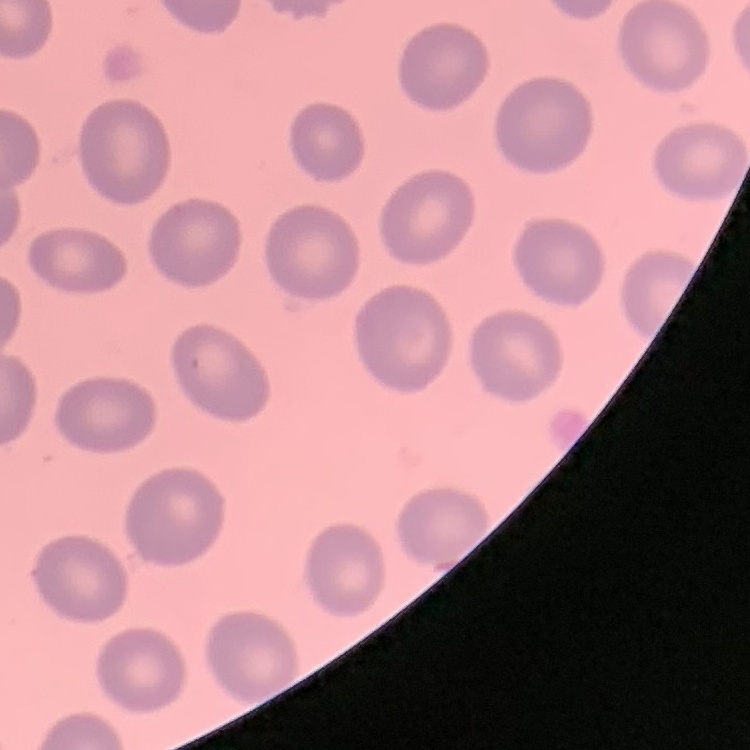

{
  "erythrocyte_morphology": "no rouleaux formation",
  "preparation": "thin blood film",
  "image_type": "square crop of a larger photomicrograph",
  "stain": "Field's or Giemsa"
}